Outline each Plasmodium ovale-infected red blood cell.
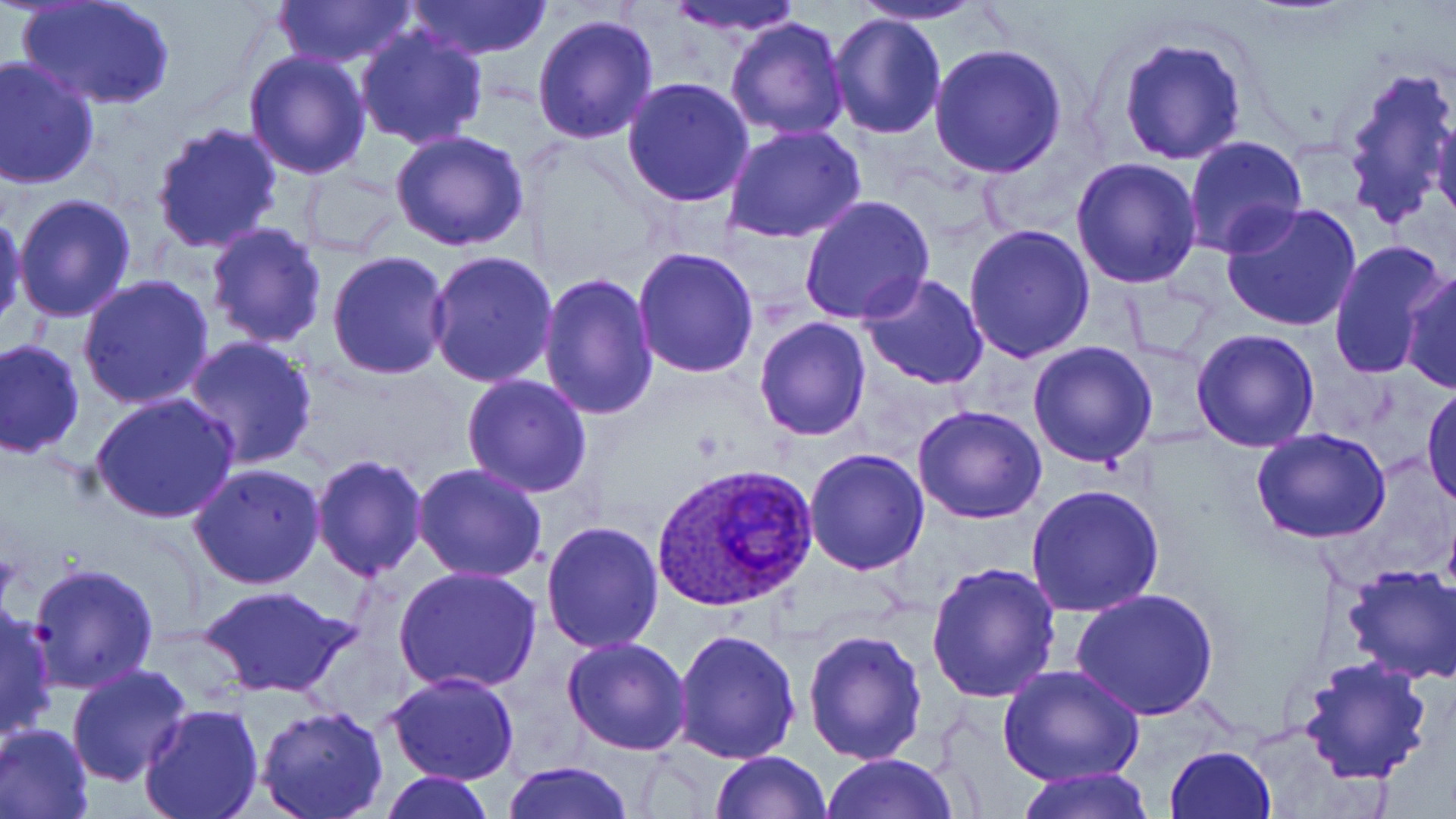

Approximate bounding boxes as named x1/y1/x2/y2 corners in pixels.
Plasmodium ovale-infected red blood cells: (x1=654, y1=462, x2=818, y2=613).

Summary:
  - Uninfected red blood cell locations: (x1=271, y1=0, x2=418, y2=70), (x1=406, y1=0, x2=553, y2=62), (x1=664, y1=0, x2=811, y2=37), (x1=849, y1=0, x2=990, y2=25), (x1=19, y1=1, x2=173, y2=111), (x1=828, y1=11, x2=946, y2=138), (x1=531, y1=13, x2=659, y2=144), (x1=723, y1=16, x2=850, y2=140), (x1=355, y1=26, x2=490, y2=150), (x1=1118, y1=37, x2=1248, y2=165), (x1=929, y1=43, x2=1067, y2=178), (x1=242, y1=48, x2=372, y2=178), (x1=0, y1=57, x2=101, y2=190), (x1=1337, y1=60, x2=1455, y2=234), (x1=622, y1=77, x2=755, y2=209), (x1=1431, y1=110, x2=1456, y2=230), (x1=150, y1=120, x2=283, y2=252), (x1=723, y1=125, x2=866, y2=244), (x1=389, y1=129, x2=530, y2=253), (x1=1185, y1=136, x2=1308, y2=258), (x1=1071, y1=156, x2=1203, y2=289), (x1=299, y1=166, x2=407, y2=257), (x1=12, y1=192, x2=139, y2=323), (x1=800, y1=195, x2=935, y2=324), (x1=1220, y1=201, x2=1362, y2=333), (x1=0, y1=210, x2=26, y2=331), (x1=204, y1=223, x2=330, y2=351), (x1=963, y1=223, x2=1096, y2=362), (x1=1330, y1=239, x2=1452, y2=380), (x1=632, y1=246, x2=761, y2=378), (x1=326, y1=250, x2=453, y2=379), (x1=426, y1=251, x2=559, y2=388), (x1=868, y1=254, x2=1088, y2=380), (x1=1400, y1=267, x2=1454, y2=395), (x1=536, y1=272, x2=659, y2=420), (x1=857, y1=272, x2=989, y2=390), (x1=76, y1=274, x2=217, y2=411), (x1=754, y1=318, x2=872, y2=440), (x1=1191, y1=328, x2=1321, y2=453), (x1=180, y1=336, x2=319, y2=471), (x1=0, y1=339, x2=85, y2=459), (x1=1027, y1=341, x2=1159, y2=468), (x1=462, y1=373, x2=593, y2=497), (x1=1422, y1=382, x2=1456, y2=510), (x1=89, y1=391, x2=241, y2=524), (x1=912, y1=405, x2=1047, y2=524), (x1=1251, y1=428, x2=1394, y2=545), (x1=803, y1=448, x2=930, y2=575), (x1=309, y1=455, x2=429, y2=582), (x1=188, y1=462, x2=328, y2=589), (x1=411, y1=463, x2=552, y2=585), (x1=1024, y1=483, x2=1167, y2=616), (x1=541, y1=519, x2=667, y2=653), (x1=28, y1=563, x2=160, y2=692), (x1=924, y1=563, x2=1064, y2=705), (x1=1341, y1=564, x2=1456, y2=685), (x1=392, y1=566, x2=543, y2=696), (x1=196, y1=583, x2=354, y2=698), (x1=1071, y1=589, x2=1217, y2=720), (x1=0, y1=603, x2=57, y2=744), (x1=672, y1=626, x2=802, y2=763), (x1=802, y1=627, x2=928, y2=764), (x1=563, y1=635, x2=693, y2=755), (x1=1297, y1=654, x2=1433, y2=787), (x1=67, y1=663, x2=194, y2=787), (x1=1000, y1=666, x2=1142, y2=788), (x1=383, y1=671, x2=520, y2=785), (x1=139, y1=704, x2=265, y2=819), (x1=254, y1=706, x2=388, y2=819), (x1=1, y1=722, x2=94, y2=819), (x1=1163, y1=745, x2=1276, y2=819), (x1=709, y1=749, x2=833, y2=818), (x1=822, y1=753, x2=958, y2=819), (x1=501, y1=761, x2=635, y2=819), (x1=1009, y1=769, x2=1155, y2=819), (x1=379, y1=772, x2=495, y2=818)
  - Slide-level diagnosis: Plasmodium ovale
  - Image size: 1456×819 pixels
  - Field of view: single
  - Magnification: 1000x
  - Stain: May-Grünwald-Giemsa
  - Modality: optical microscopy
  - Preparation: thin blood smear